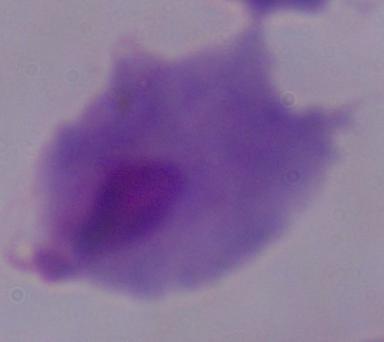
Summary:
  - Modality: photomicrograph
  - Identification: trichomonad
  - Magnification: 1000x